Identify the blood parasite species.
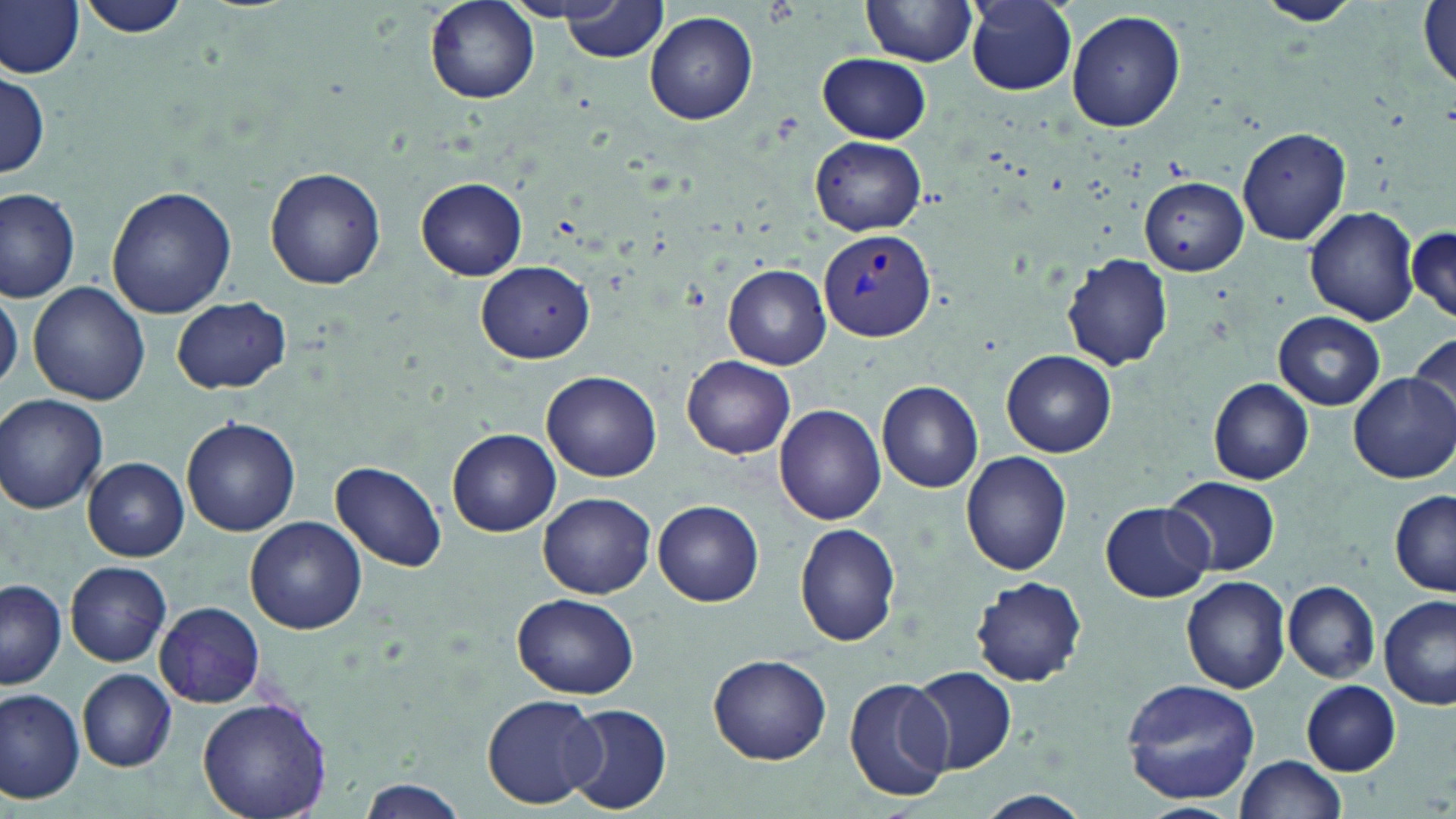

Plasmodium vivax.

Summary:
  - Coordinate format: approximate bounding boxes as (x1,y1)-(x2,y2) corner pairs in pixels
  - Uninfected red blood cell locations: (1257,0)-(1360,25), (0,1)-(84,79), (424,1)-(538,105), (861,1)-(977,68), (965,1)-(1078,95), (80,2)-(193,41), (558,2)-(667,63), (1418,2)-(1455,91), (1065,9)-(1185,132), (644,11)-(757,125), (818,53)-(930,143), (0,73)-(49,181), (1237,126)-(1351,246), (811,136)-(927,235), (266,167)-(385,289), (416,178)-(527,279), (1140,178)-(1247,274), (107,186)-(236,319), (0,188)-(81,301), (1305,206)-(1419,325), (1409,225)-(1455,322), (1063,254)-(1173,370), (478,261)-(595,361), (724,264)-(832,369), (27,282)-(149,406), (0,289)-(22,393), (171,296)-(290,393), (1274,312)-(1385,410), (1408,333)-(1456,427), (1001,351)-(1115,458), (682,355)-(796,458), (542,369)-(661,482), (1350,376)-(1456,482), (1208,379)-(1314,485), (877,381)-(985,493), (0,394)-(108,513), (774,404)-(886,526), (183,419)-(301,537), (448,430)-(560,537), (960,450)-(1072,577), (83,459)-(188,560), (331,460)-(447,571), (1165,475)-(1281,576), (538,491)-(656,599), (1390,491)-(1456,596), (653,501)-(764,606), (1101,502)-(1212,602), (245,517)-(366,634), (794,523)-(902,646), (66,561)-(172,667), (1180,574)-(1291,693), (970,576)-(1087,686), (1,580)-(65,690), (1283,581)-(1379,682), (512,593)-(640,698), (1380,597)-(1456,709), (155,601)-(265,706), (707,653)-(832,766), (909,666)-(1017,775), (78,670)-(176,771), (844,675)-(953,802), (1121,678)-(1262,806), (1301,679)-(1401,775), (0,689)-(85,803), (480,692)-(605,809), (195,698)-(333,819), (563,704)-(672,815), (1235,754)-(1345,819), (357,778)-(467,819), (976,791)-(1090,819), (1135,803)-(1244,819)
  - Plasmodium vivax-infected red blood cell locations: (818,230)-(935,342)
  - Modality: optical microscopy
  - Field of view: single
  - Magnification: 1000x
  - Preparation: thin blood smear
  - Stain: May-Grünwald-Giemsa
  - Image size: 1456×819 pixels